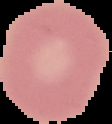

Cell region segmented out of the field of view; the surrounding area is masked to black. From a thin blood smear. Result: negative for Plasmodium parasites. Image is 112×124 pixels.